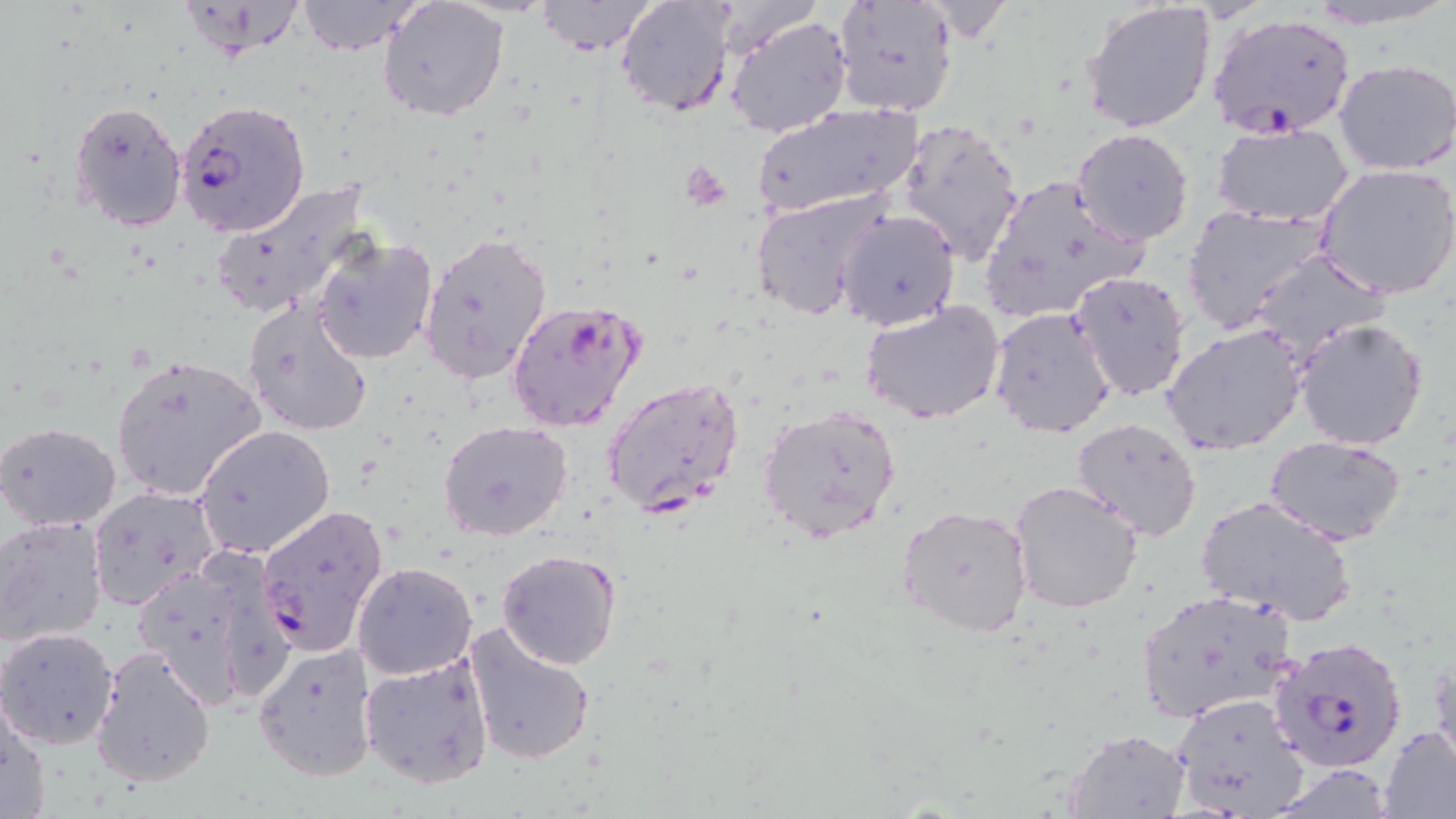
Plasmodium falciparum-infected red blood cell locations = approximate bounding boxes as (x1, y1, x2, y2) in pixels: (1206, 11, 1358, 140), (175, 99, 311, 237), (507, 297, 646, 431), (602, 376, 746, 518), (255, 502, 390, 658), (1268, 637, 1406, 776)
slide-level diagnosis = Plasmodium falciparum
platelet locations = approximate bounding boxes as (x1, y1, x2, y2) in pixels: (682, 161, 730, 210)
preparation = thin blood film
image size = 1456×819 pixels
magnification = 1000x
field of view = one of a larger specimen
stain = May-Grünwald-Giemsa
uninfected red blood cell locations = approximate bounding boxes as (x1, y1, x2, y2) in pixels: (183, 0, 308, 61), (536, 0, 659, 56), (615, 0, 737, 119), (831, 0, 958, 118), (1304, 0, 1456, 27), (295, 1, 420, 56), (377, 1, 510, 121), (1081, 1, 1219, 135), (726, 15, 854, 138), (1332, 58, 1456, 173), (69, 99, 188, 232), (750, 103, 925, 220), (897, 120, 1025, 265), (1209, 122, 1358, 229), (1071, 128, 1196, 246), (1315, 164, 1456, 300), (974, 172, 1152, 327), (209, 178, 372, 322), (750, 190, 892, 321), (1180, 204, 1333, 334), (835, 209, 960, 331), (418, 231, 552, 385), (311, 234, 438, 365), (1245, 248, 1391, 365), (1066, 272, 1192, 404), (243, 297, 374, 437), (860, 301, 1007, 425), (988, 306, 1116, 440), (1292, 316, 1431, 451), (1162, 323, 1308, 456), (110, 355, 268, 501), (757, 403, 903, 542), (1070, 417, 1203, 539), (438, 421, 571, 542), (0, 422, 122, 532), (195, 424, 336, 558), (1266, 436, 1407, 545), (1010, 478, 1145, 614), (87, 484, 220, 610), (1193, 493, 1359, 630), (898, 503, 1033, 637), (0, 516, 109, 645), (495, 547, 621, 669), (131, 557, 266, 710), (352, 562, 476, 681), (1133, 587, 1300, 724), (464, 621, 597, 765), (0, 627, 120, 747), (253, 642, 378, 782), (90, 644, 216, 788), (359, 653, 495, 791), (1171, 691, 1313, 818), (0, 697, 50, 819), (1379, 723, 1456, 819), (1062, 730, 1192, 817)
modality = light microscopy